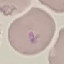
Summary:
  - Result: malaria parasites detected
  - Stain: Giemsa
  - Preparation: thin smear
  - Capture: smartphone camera at the microscope eyepiece
  - Image type: automatically extracted cell patch, resized to 64 × 64 pixels